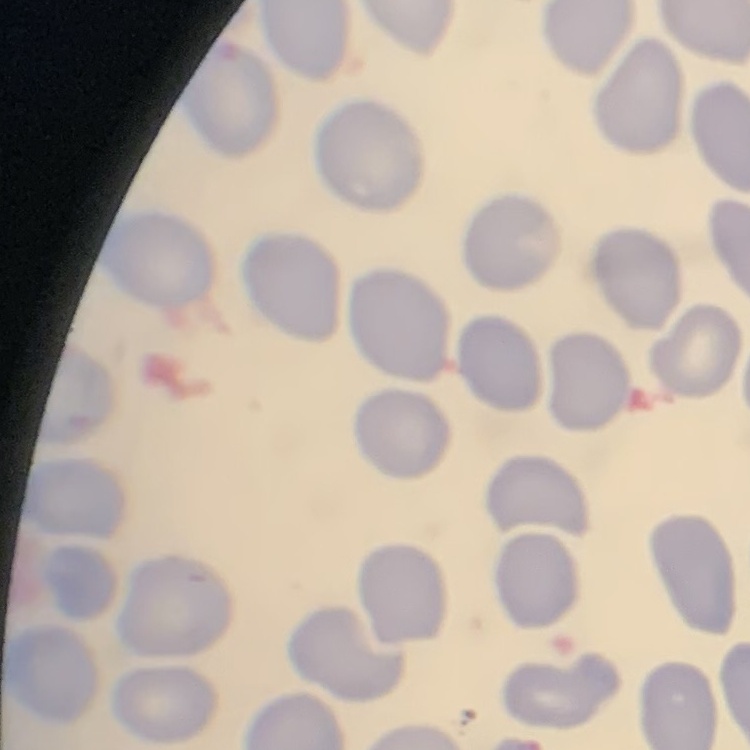

Summary:
  - Erythrocyte morphology: no rouleaux formation
  - Image type: square crop of a larger photomicrograph
  - Stain: Field's or Giemsa
  - Preparation: thin peripheral smear